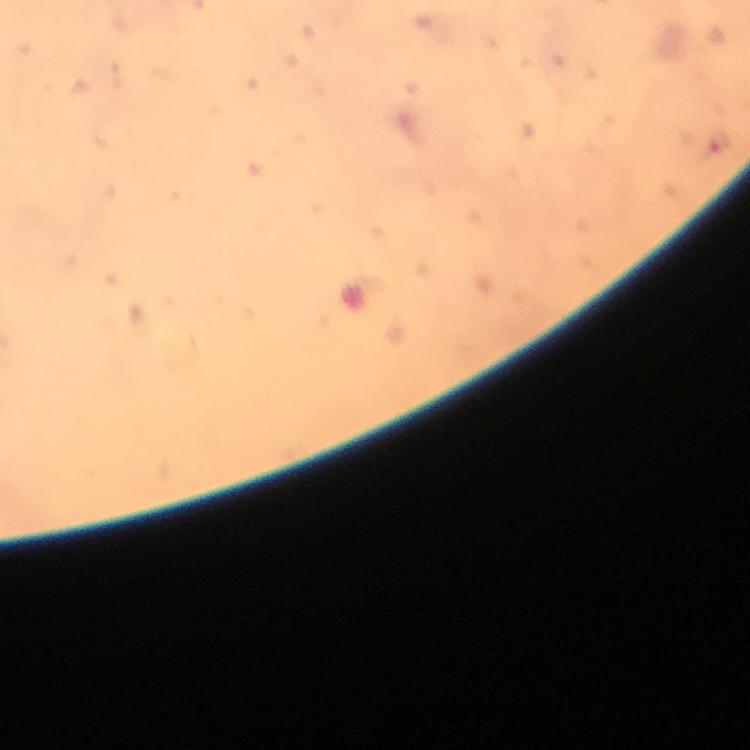 Approximate object centers, in pixels from the top-left corner. Malaria parasite locations: (x=717, y=141). Photographed through the microscope with a smartphone camera. Immersion oil was used. From a malaria diagnostic workup. A crop from one field of view. Thick smear. Giemsa-stained preparation. At 100x magnification. Image is 750×750 pixels.